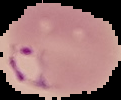
preparation = thin blood film
image size = 121×100 pixels
image type = cell region segmented out of the field of view; surrounding area masked to black
malaria status = parasitized